Describe the morphology of the erythrocytes.
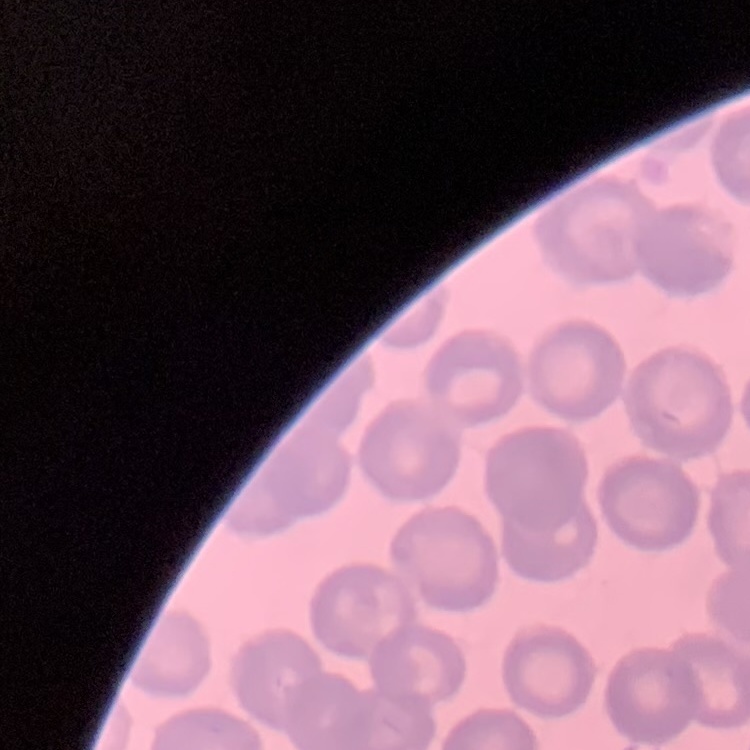

No rouleaux formation.

stain: Field's or Giemsa
preparation: thin blood film
image_type: square crop of a larger photomicrograph